Identify the parasite.
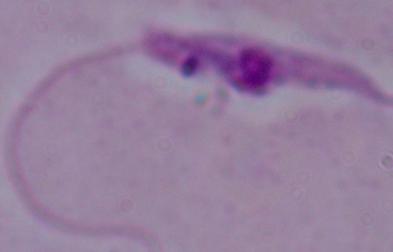
This is Leishmania.

1000x magnification. Photomicrograph.